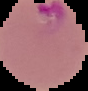 From a thin blood film. Image is 88×91 pixels. Segmented cell region on a black background. Result: Plasmodium parasites detected.